Assess for malaria.
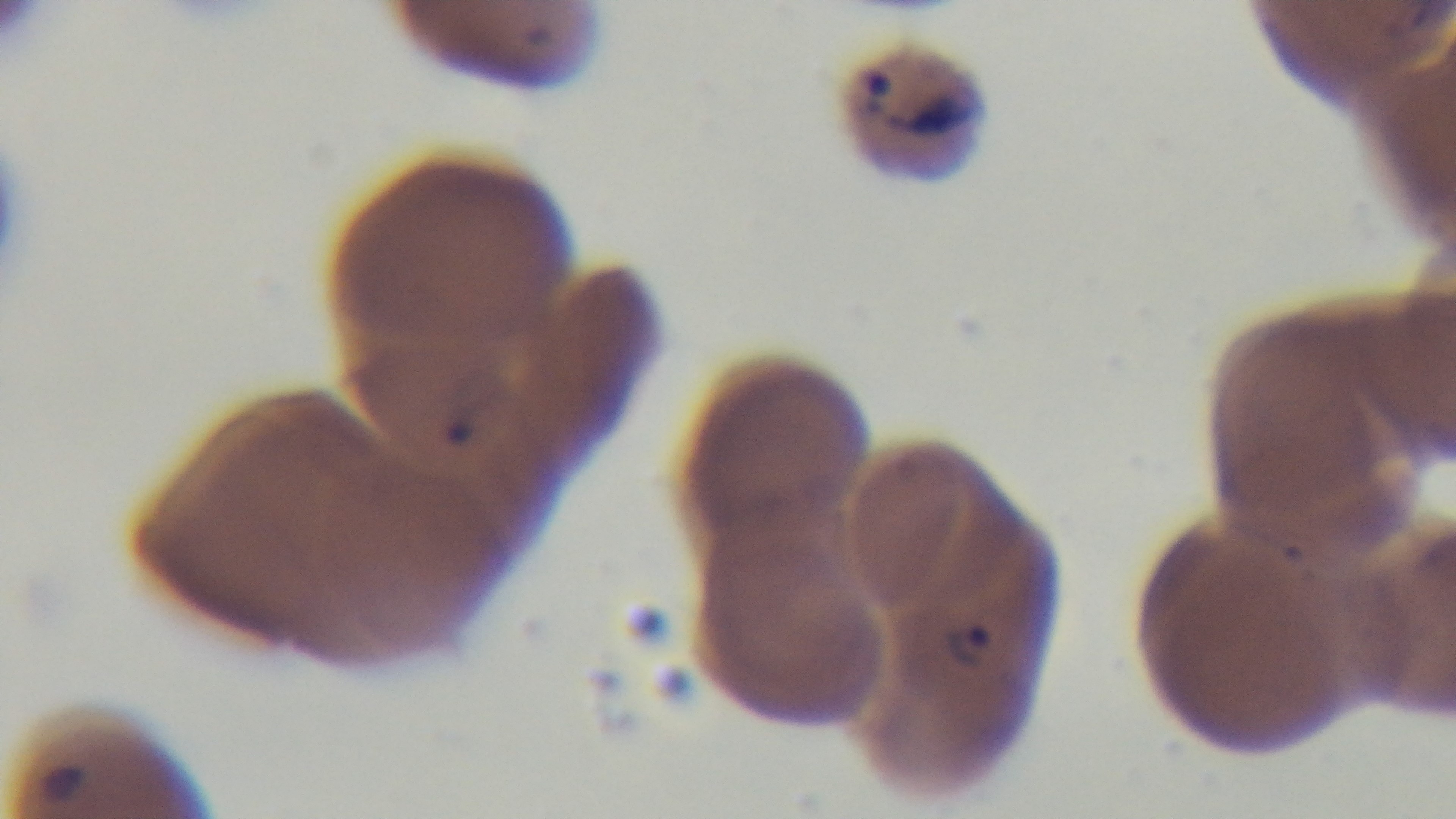

It is infected.

Single field of view. Mounted 4K digital camera. 100x oil-immersion objective. Photomicrograph. Giemsa-stained. Preparation: thin smear.